State the blood parasite species.
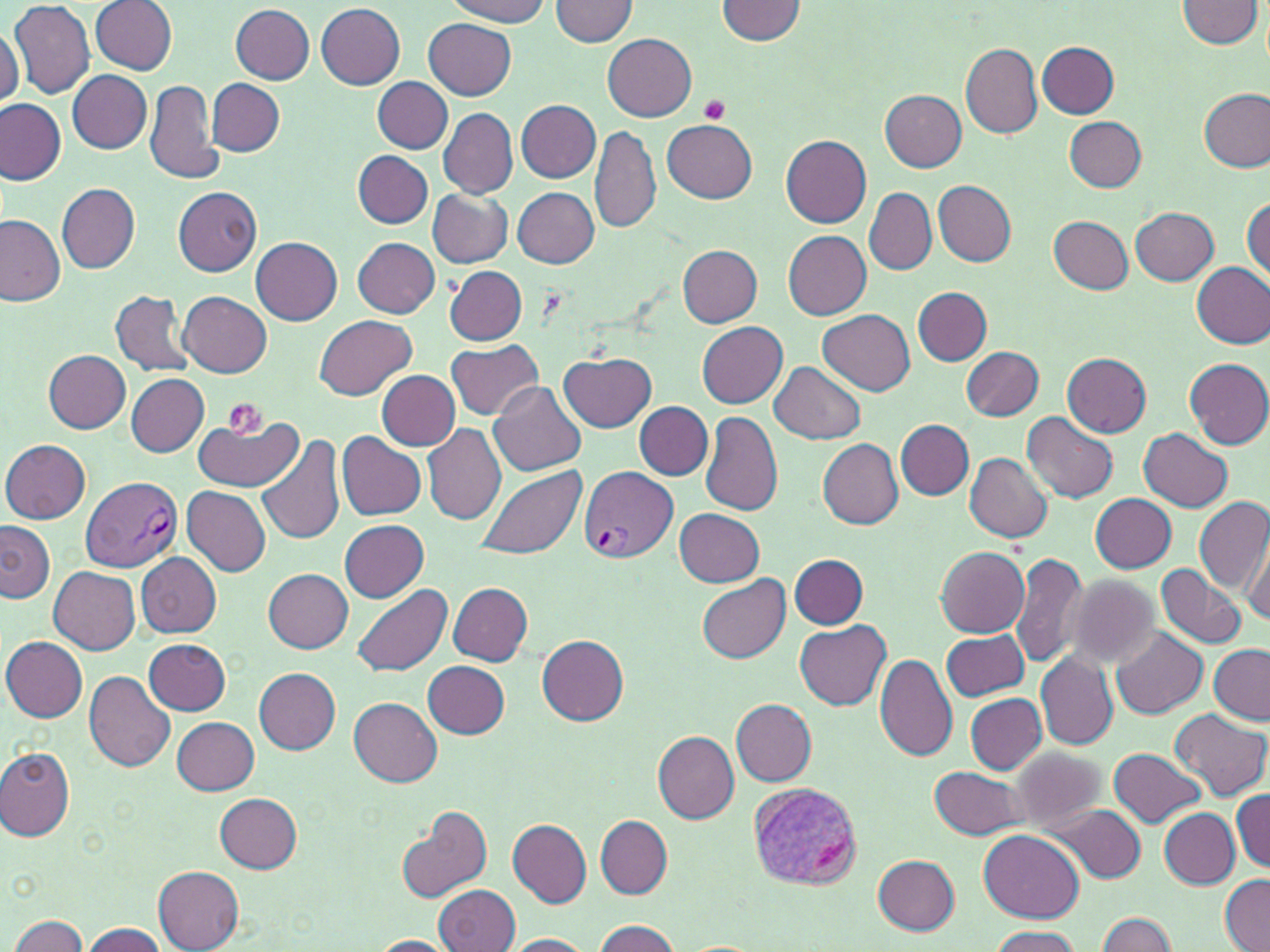
Plasmodium vivax.

Summary:
  - Coordinate format: approximate bounding boxes as [x1, y1, x2, y2] in pixels
  - Platelet locations: [698, 95, 730, 126], [220, 398, 268, 442]
  - Plasmodium vivax-infected red blood cell locations: [579, 466, 678, 562], [82, 477, 182, 571], [747, 783, 861, 890]
  - Uninfected red blood cell locations: [447, 0, 550, 25], [548, 0, 639, 46], [717, 0, 807, 43], [1177, 0, 1262, 48], [8, 1, 95, 100], [90, 1, 176, 74], [315, 3, 405, 89], [231, 5, 315, 84], [423, 19, 515, 100], [1, 24, 23, 107], [603, 34, 696, 121], [1038, 41, 1119, 118], [962, 43, 1042, 138], [67, 70, 151, 153], [208, 78, 285, 154], [373, 78, 454, 152], [145, 79, 223, 187], [1199, 88, 1270, 174], [881, 91, 967, 171], [0, 100, 66, 184], [516, 100, 601, 181], [439, 108, 518, 198], [1065, 117, 1146, 191], [661, 119, 757, 203], [590, 125, 661, 235], [781, 135, 872, 229], [353, 150, 432, 228], [933, 181, 1016, 265], [57, 184, 140, 272], [174, 186, 262, 277], [513, 187, 598, 268], [865, 188, 935, 275], [426, 189, 514, 268], [1245, 195, 1270, 283], [1130, 206, 1219, 286], [0, 214, 67, 307], [1048, 216, 1132, 294], [784, 231, 872, 320], [250, 237, 342, 325], [352, 237, 440, 317], [676, 244, 763, 325], [1192, 262, 1270, 349], [446, 266, 526, 345], [914, 287, 992, 365], [111, 289, 194, 377], [179, 292, 272, 378], [819, 311, 915, 396], [316, 315, 416, 399], [696, 321, 788, 405], [445, 340, 544, 421], [963, 346, 1044, 421], [44, 350, 130, 432], [560, 351, 657, 432], [1063, 352, 1151, 437], [1186, 359, 1270, 447], [770, 362, 865, 444], [376, 370, 460, 450], [126, 374, 208, 456], [489, 381, 586, 477], [634, 401, 713, 479], [1022, 410, 1117, 503], [700, 411, 782, 517], [190, 413, 304, 490], [896, 419, 973, 500], [423, 423, 506, 524], [1138, 429, 1233, 512], [256, 432, 347, 546], [337, 433, 426, 520], [1, 439, 90, 524], [818, 439, 904, 529], [964, 453, 1053, 542], [475, 464, 586, 560], [182, 486, 272, 576], [1090, 493, 1177, 573], [1194, 497, 1270, 593], [681, 505, 775, 663], [675, 508, 765, 587], [340, 519, 429, 603], [0, 520, 55, 603], [1243, 533, 1270, 630], [936, 547, 1028, 638], [1008, 551, 1090, 668], [136, 552, 221, 637], [791, 554, 869, 628], [1156, 564, 1247, 649], [48, 566, 140, 653], [264, 569, 352, 652], [696, 572, 790, 661], [1063, 574, 1162, 671], [448, 582, 534, 665], [353, 585, 453, 677], [795, 621, 891, 712], [1111, 627, 1208, 718], [942, 629, 1029, 701], [536, 634, 629, 725], [1, 636, 87, 722], [143, 638, 231, 714], [1209, 645, 1270, 725], [1036, 653, 1117, 750], [875, 654, 957, 762], [424, 660, 510, 738], [254, 667, 341, 754], [83, 671, 177, 772], [965, 694, 1047, 774], [348, 698, 442, 786], [731, 698, 815, 785], [1169, 709, 1267, 802], [172, 717, 259, 796], [652, 729, 739, 822], [1007, 746, 1105, 833], [0, 748, 75, 841], [1110, 748, 1207, 827], [930, 765, 1029, 841], [1232, 791, 1269, 872], [214, 793, 303, 872], [396, 804, 492, 905], [1054, 805, 1145, 882], [1160, 808, 1239, 888], [596, 816, 672, 899], [507, 819, 591, 907], [979, 830, 1085, 924], [874, 854, 960, 935], [155, 867, 245, 952], [1220, 873, 1269, 952], [434, 884, 520, 952], [1096, 912, 1178, 951], [8, 915, 87, 951], [591, 919, 682, 952], [82, 922, 170, 952], [987, 926, 1082, 952], [501, 934, 596, 952], [365, 935, 458, 951]
  - Stain: May-Grünwald-Giemsa
  - Modality: light microscopy
  - Magnification: 1000x
  - Image size: 1270×952 pixels
  - Preparation: thin blood film
  - Field of view: one of a larger specimen